Identify the blood parasite species.
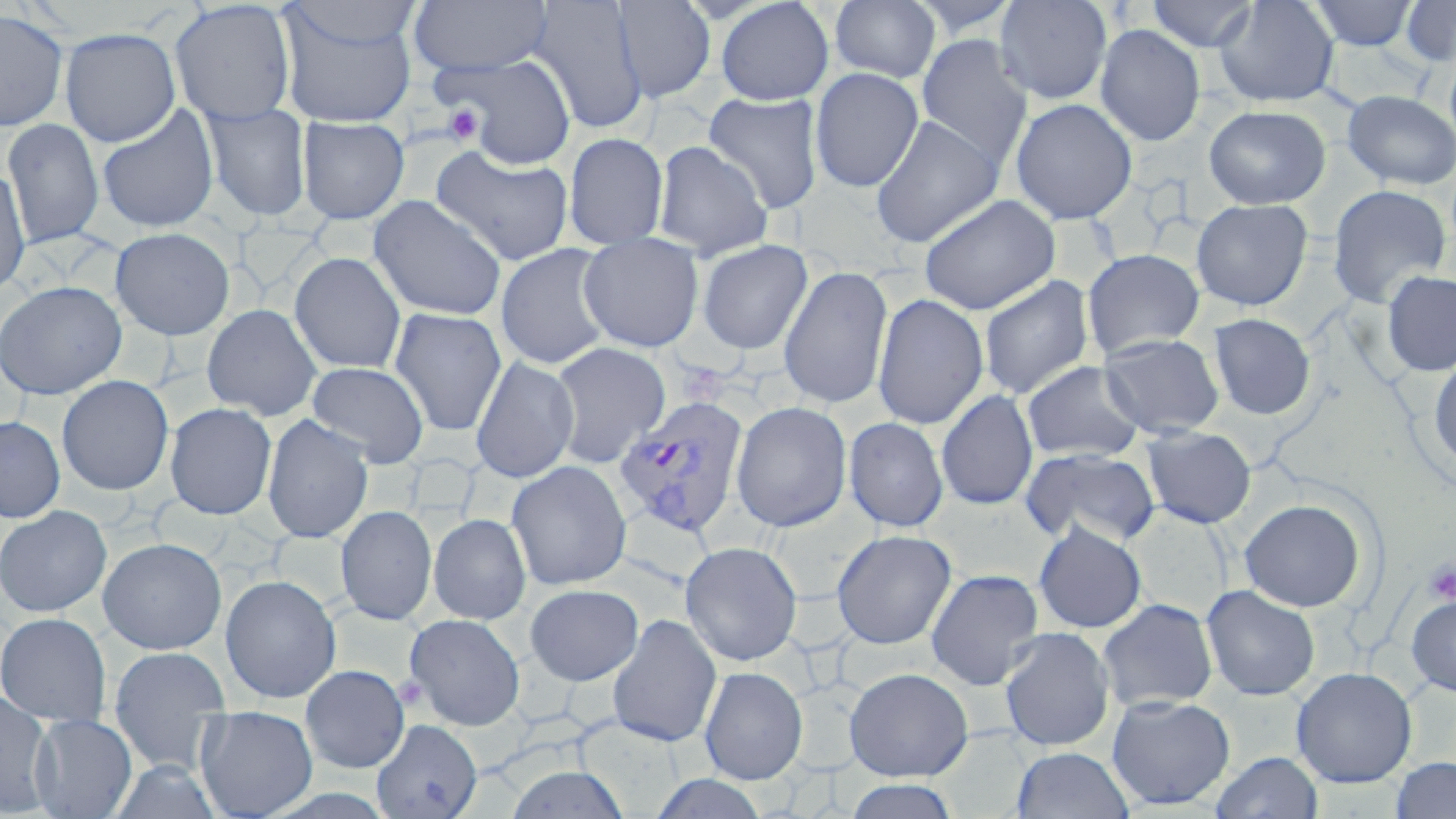

Plasmodium vivax.

Approximate bounding boxes as (x1,y1)-(x2,y2) corner pairs in pixels. Platelet locations: (440,102)-(486,148), (1424,559)-(1456,605), (395,674)-(428,710). Uninfected red blood cell locations: (528,0)-(648,134), (612,0)-(716,103), (830,0)-(941,83), (907,0)-(1021,39), (994,0)-(1113,105), (1146,0)-(1260,53), (1213,0)-(1340,108), (1309,0)-(1418,50), (1400,0)-(1456,67), (169,1)-(297,126), (409,1)-(552,78), (715,1)-(834,106), (281,2)-(423,50), (275,4)-(418,127), (0,8)-(69,131), (1095,24)-(1205,146), (59,27)-(181,147), (916,34)-(1033,170), (1445,51)-(1456,152), (439,52)-(577,170), (810,67)-(924,193), (1342,90)-(1455,190), (702,91)-(825,214), (1010,98)-(1137,225), (202,102)-(311,222), (97,104)-(220,233), (1203,105)-(1330,209), (870,115)-(1003,248), (297,116)-(409,224), (2,119)-(104,249), (564,132)-(669,250), (651,140)-(774,261), (431,145)-(574,266), (0,166)-(31,296), (1327,184)-(1451,309), (918,194)-(1061,315), (368,195)-(507,321), (1191,198)-(1313,311), (110,227)-(235,340), (578,233)-(704,352), (697,239)-(813,355), (495,243)-(616,370), (1082,249)-(1204,359), (290,253)-(406,374), (777,265)-(893,410), (1381,271)-(1456,377), (979,274)-(1095,399), (0,280)-(127,400), (872,293)-(989,429), (201,303)-(322,421), (388,308)-(507,436), (1208,313)-(1315,420), (1098,333)-(1225,439), (549,342)-(671,468), (1427,355)-(1456,475), (470,356)-(579,483), (1021,360)-(1146,462), (307,361)-(430,468), (56,375)-(174,495), (935,389)-(1039,510), (731,401)-(852,532), (164,402)-(277,520), (262,415)-(373,543), (0,416)-(66,523), (843,416)-(949,533), (1141,426)-(1256,529), (1020,448)-(1161,549), (506,460)-(632,590), (1239,498)-(1367,612), (0,505)-(112,617), (335,505)-(437,625), (428,513)-(531,624), (1033,522)-(1147,633), (831,529)-(956,649), (97,537)-(227,654), (680,541)-(802,666), (925,568)-(1044,691), (220,574)-(341,704), (525,583)-(643,686), (1201,585)-(1320,701), (1405,593)-(1456,697), (1097,598)-(1218,712), (1037,607)-(1171,725), (0,611)-(111,727), (404,613)-(525,730), (608,614)-(722,748), (999,626)-(1115,751), (108,646)-(231,772), (300,664)-(410,773), (699,666)-(808,784), (1291,666)-(1418,787), (844,667)-(973,782), (0,690)-(55,816), (1106,694)-(1235,810), (194,705)-(318,819), (28,714)-(137,818), (371,717)-(482,818), (1011,746)-(1133,819), (1211,751)-(1323,819), (1390,756)-(1456,818), (507,764)-(629,819), (651,773)-(769,818), (844,778)-(961,819). Plasmodium vivax-infected red blood cell locations: (613,395)-(749,538). Captured at 1000x magnification. One field of a larger specimen. May-Grünwald-Giemsa stain. Thin blood smear. Optical microscopy. Image is 1456×819 pixels.